Give the position of every malaria parasite.
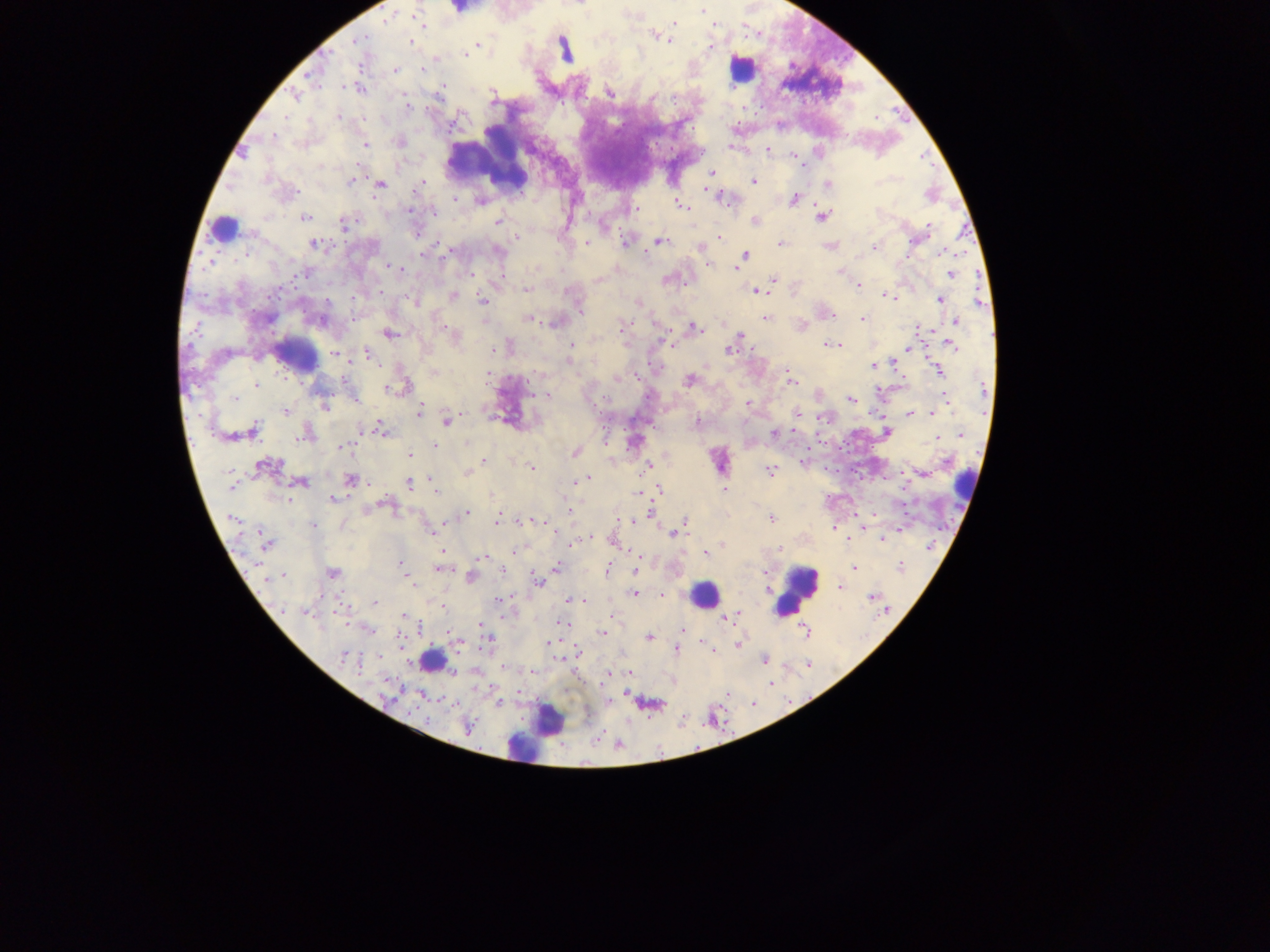
Approximate centers as x y in pixels.
Malaria parasites: 456 9; 700 11; 674 22; 715 26; 653 36; 358 43; 409 43; 478 43; 671 43; 562 48; 465 54; 395 70; 579 82; 442 87; 361 89; 491 93; 609 93; 404 95; 408 107; 287 116; 338 116; 272 136; 365 146; 730 148; 767 150; 247 155; 794 155; 710 171; 423 181; 753 181; 351 183; 876 183; 828 185; 380 186; 296 191; 715 193; 794 198; 455 202; 681 205; 409 208; 634 210; 820 217; 306 218; 755 219; 498 221; 565 222; 344 224; 928 227; 222 230; 721 236; 518 237; 626 241; 660 241; 313 243; 434 243; 586 243; 781 243; 909 245; 700 248; 875 248; 745 254; 209 261; 382 265; 708 265; 391 266; 736 266; 712 267; 401 270; 839 272; 301 273; 471 274; 950 274; 774 278; 860 286; 526 289; 755 292; 761 292; 453 295; 886 297; 940 298; 482 299; 414 302; 639 303; 578 308; 765 318; 861 318; 529 319; 956 319; 622 324; 697 327; 932 331; 391 333; 740 336; 828 343; 823 344; 840 344; 950 344; 573 347; 493 349; 909 349; 727 350; 333 352; 370 354; 873 366; 787 369; 433 372; 943 372; 488 375; 618 378; 688 379; 790 383; 258 385; 256 388; 385 388; 392 388; 191 393; 546 394; 530 395; 946 396; 234 399; 850 401; 949 401; 749 403; 323 406; 285 412; 797 414; 938 414; 420 415; 911 415; 932 415; 467 416; 503 418; 697 421; 447 422; 382 427; 255 428; 252 431; 773 431; 797 432; 223 433; 887 433; 961 434; 303 439; 938 440; 465 444; 344 445; 433 445; 337 446; 575 454; 410 456; 485 461; 261 464; 649 465; 257 468; 531 468; 767 468; 466 472; 770 472; 589 478; 430 479; 350 480; 574 482; 408 483; 303 484; 231 487; 725 488; 659 489; 436 491; 334 500; 386 503; 377 506; 367 510; 568 512; 467 513; 231 519; 772 519; 498 520; 685 521; 541 522; 446 523; 521 523; 312 525; 550 525; 902 528; 862 529; 431 533; 669 533; 590 537; 882 539; 571 544; 266 545; 513 550; 440 552; 704 552; 482 559; 401 563; 637 566; 899 566; 556 567; 607 567; 439 568; 853 568; 445 570; 331 574; 284 576; 410 582; 538 583; 840 587; 767 590; 636 593; 661 596; 870 597; 497 600; 567 600; 581 600; 586 600; 375 601; 441 609; 304 613; 611 615; 404 616; 723 619; 479 625; 682 631; 603 633; 450 635; 648 638; 549 642; 676 648; 577 649; 342 654; 379 656; 630 673; 421 698; 498 704; 467 726.

leukocyte locations = approximate centers as x y in pixels: 742 73; 491 152; 297 355; 798 592; 706 596; 437 665; 550 720; 523 747
image size = 1270×952 pixels
field of view = single
country = Ghana
preparation = thick blood smear
capture = mobile-phone photograph through a microscope